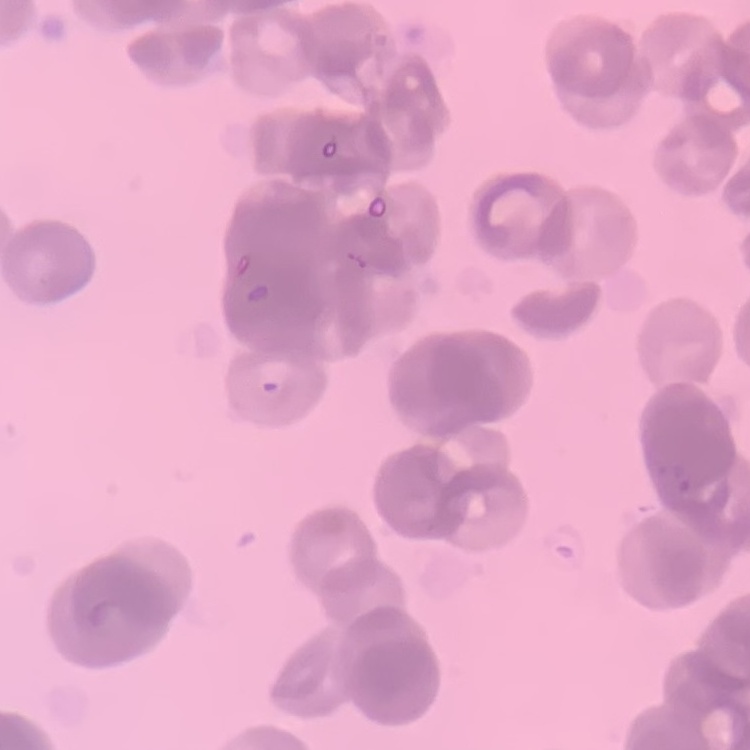

erythrocyte_morphology: rouleaux formation
stain: Field's or Giemsa
image_type: square crop of a larger photomicrograph
preparation: thin peripheral smear